Report the malaria status of this cell.
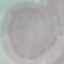

Uninfected.

Acquired by smartphone through the microscope eyepiece. Cell patch, automatically extracted from a larger field of view and resized to 64 × 64 pixels. Giemsa-stained preparation. Thin blood film.